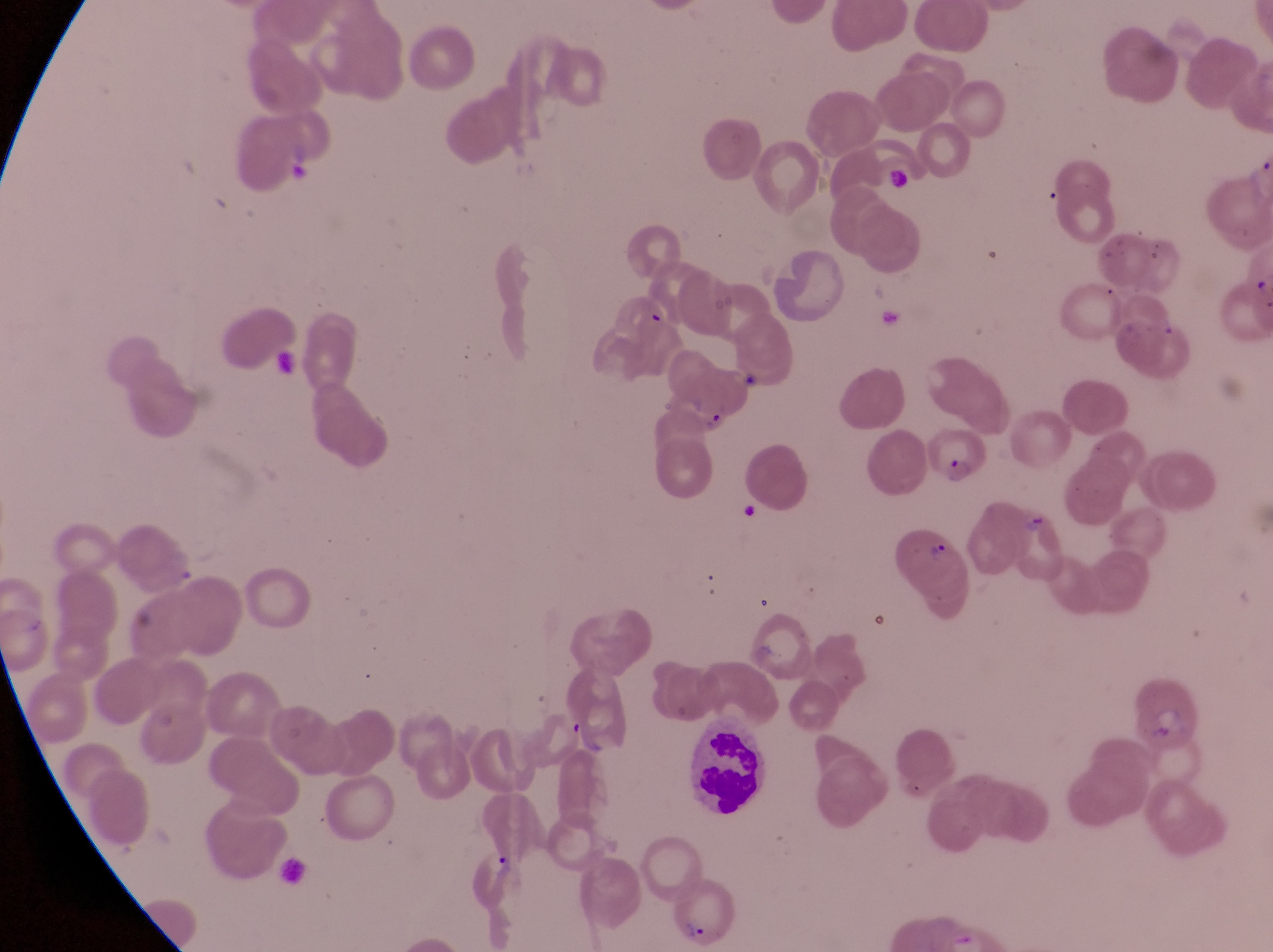

Approximate bounding boxes as [left, top, right, bottom] in pixels.
Summary:
  - Trophozoite locations: [487, 844, 522, 886]
  - Leukocyte locations: [679, 717, 771, 824]
  - Parasitised red blood cell locations: [929, 422, 989, 487], [891, 515, 969, 597], [671, 869, 743, 947]
  - Artifact (platelet-like body, stain precipitate, or debris) locations: [884, 165, 914, 192], [697, 407, 732, 439], [1025, 510, 1055, 542]
  - Image size: 1273×952 pixels
  - Preparation: thin blood film
  - Country: Uganda
  - Field of view: single
  - Magnification: 1000x
  - Capture: smartphone photograph through the eyepiece of an Olympus CX-23 microscope